Report the malaria status of this cell.
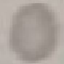
It is uninfected.

Thin blood film. Automatically extracted cell patch, resized to 64 × 64 pixels. Acquired by smartphone through the microscope eyepiece. Giemsa-stained preparation.